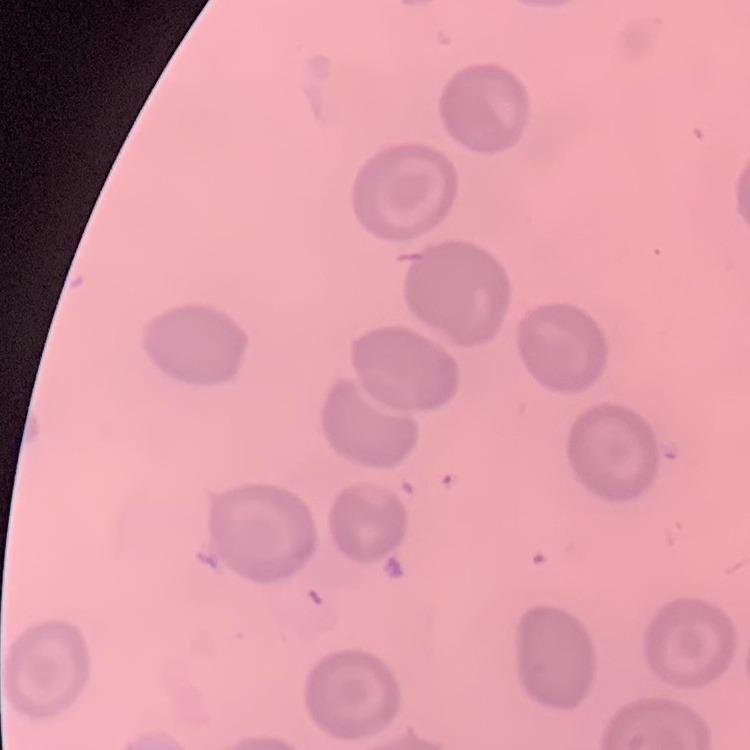
Summary:
  - Erythrocyte morphology: no rouleaux formation
  - Image type: square crop of a larger photomicrograph
  - Preparation: thin peripheral smear
  - Stain: Field's or Giemsa